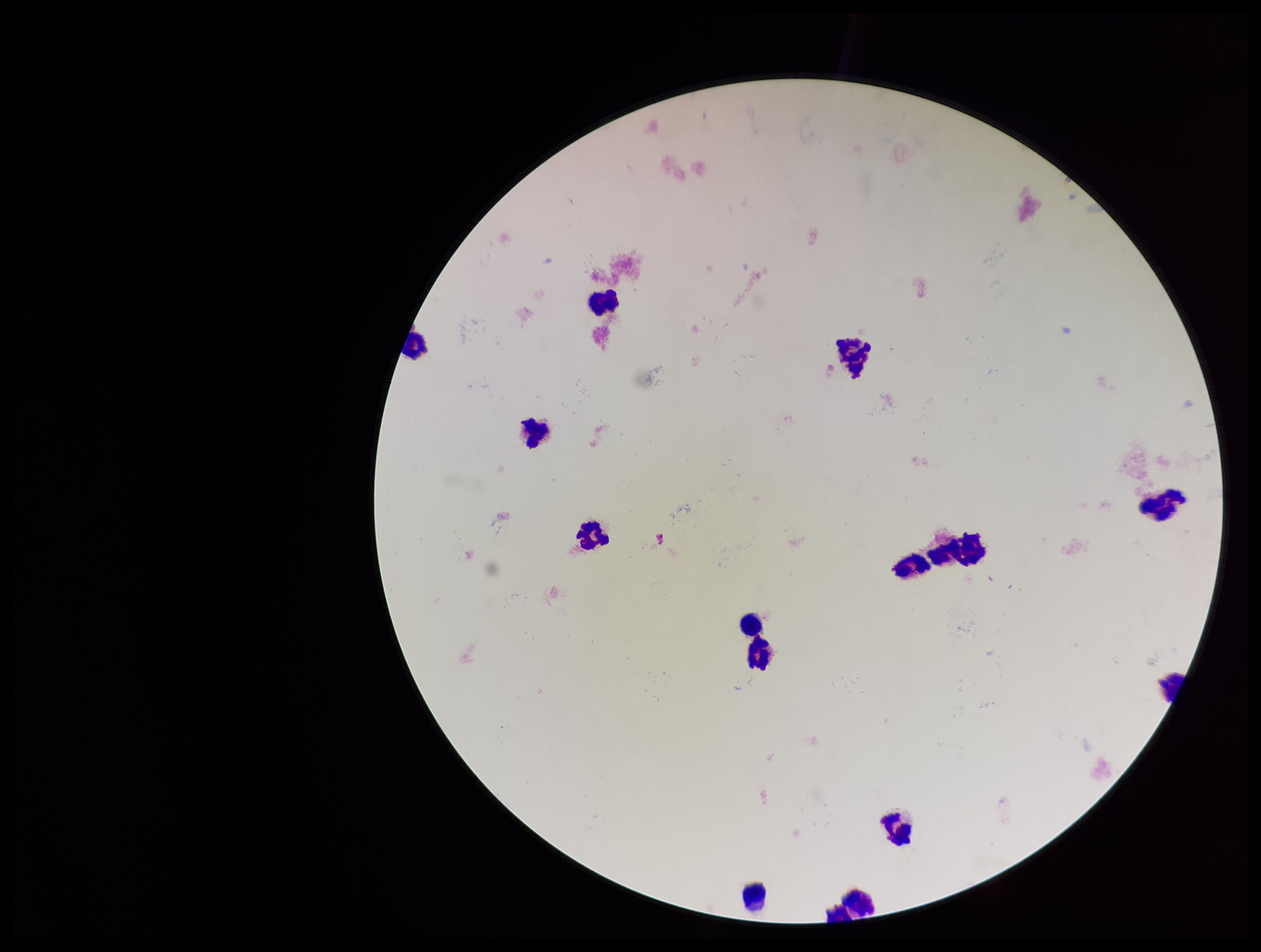
{
  "stain": "Giemsa",
  "patient_malaria_status": "negative",
  "leukocyte_count": 14,
  "parasite_count": 0,
  "image_size": "1261×952 pixels",
  "capture": "smartphone photograph through the microscope eyepiece",
  "field_of_view": "one from this slide",
  "preparation": "thick smear",
  "plasmodium_parasites": "none identified"
}